Draw a bounding box around every artifact (stain precipitate or debris).
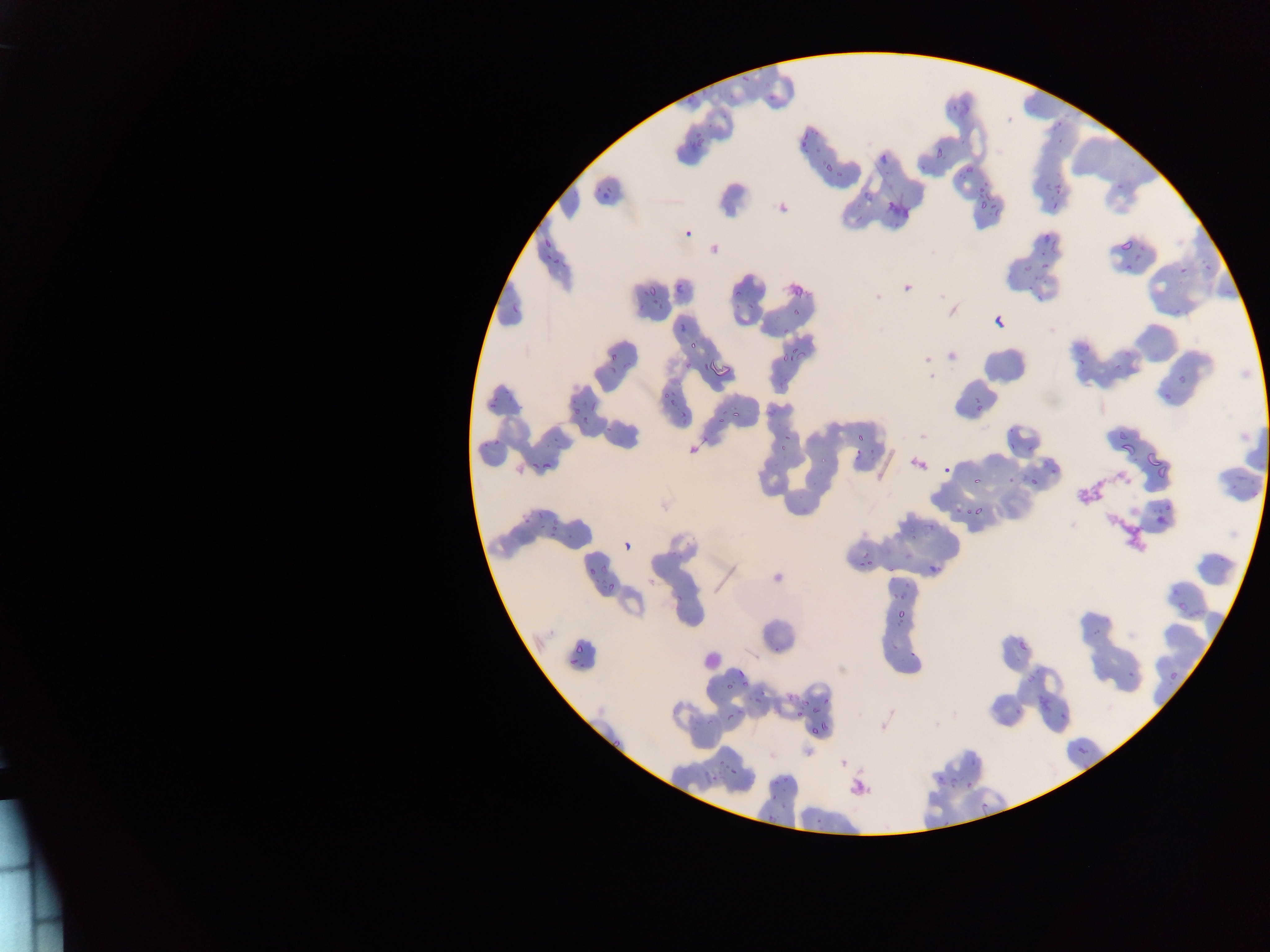

Approximate bounding boxes as (left, top, right, bottom) in pixels.
Artifacts (stain precipitate or debris): (884, 200, 908, 218), (783, 278, 806, 301), (1069, 474, 1108, 515), (1107, 510, 1150, 550), (846, 777, 868, 797).

Leukocyte locations: (700, 644, 726, 675). Malaria parasite locations: (740, 65, 756, 84), (686, 87, 704, 104), (770, 91, 777, 101), (727, 95, 737, 103), (946, 101, 960, 115), (704, 115, 719, 128), (1054, 116, 1063, 127), (686, 132, 709, 148), (794, 132, 811, 156), (1054, 135, 1062, 144), (932, 147, 944, 164), (876, 151, 890, 163), (823, 160, 838, 174), (962, 161, 983, 178), (918, 165, 927, 177), (1046, 174, 1064, 187), (596, 182, 611, 206), (976, 185, 995, 211), (861, 186, 876, 200), (1052, 202, 1060, 210), (683, 227, 694, 239), (1044, 231, 1051, 240), (1050, 235, 1061, 251), (1117, 235, 1135, 250), (544, 237, 553, 253), (543, 254, 551, 259), (551, 256, 561, 267), (1200, 259, 1211, 269), (1042, 260, 1054, 267), (1122, 264, 1132, 271), (1177, 265, 1187, 277), (675, 276, 687, 294), (639, 283, 656, 297), (1026, 283, 1034, 292), (729, 289, 741, 299), (1034, 293, 1042, 304), (651, 294, 667, 313), (744, 300, 759, 317), (511, 302, 516, 316), (1173, 302, 1183, 316), (789, 308, 803, 319), (994, 316, 1006, 329), (677, 319, 686, 331), (778, 344, 803, 369), (687, 345, 695, 351), (607, 347, 620, 360), (1075, 357, 1084, 367), (706, 360, 729, 380), (1112, 360, 1126, 372), (684, 362, 692, 370), (1175, 368, 1195, 383), (654, 379, 679, 403), (500, 391, 511, 397), (1162, 391, 1173, 400), (670, 396, 684, 414), (973, 396, 979, 404), (590, 399, 595, 410), (485, 400, 494, 409), (512, 404, 521, 411), (571, 407, 583, 415), (713, 408, 728, 430), (730, 408, 743, 422), (679, 411, 689, 423), (582, 413, 593, 424), (607, 423, 614, 431), (776, 431, 794, 454), (850, 431, 872, 455), (544, 432, 564, 445), (1007, 436, 1024, 450), (1118, 438, 1132, 453), (493, 439, 503, 444), (1028, 443, 1037, 452), (1145, 449, 1168, 468), (870, 450, 879, 462), (818, 453, 827, 463), (542, 460, 551, 467), (1152, 460, 1178, 482), (529, 461, 541, 469), (941, 464, 954, 475), (1049, 465, 1056, 474), (1029, 477, 1037, 487), (973, 481, 984, 488), (1159, 502, 1175, 514), (970, 504, 985, 518), (956, 505, 965, 513), (532, 510, 543, 522), (1153, 513, 1166, 526), (550, 514, 564, 533), (518, 518, 528, 526), (544, 524, 561, 540), (908, 527, 916, 539), (623, 541, 633, 551), (866, 556, 873, 566), (585, 558, 601, 575), (925, 560, 945, 579), (856, 561, 863, 570), (1171, 580, 1179, 593), (603, 583, 620, 593), (888, 587, 905, 601), (1177, 600, 1189, 613), (1189, 602, 1208, 620), (893, 604, 911, 623), (1014, 636, 1031, 657), (575, 638, 588, 657), (890, 641, 899, 650), (773, 645, 781, 655), (908, 648, 921, 658), (567, 660, 576, 667), (734, 668, 750, 686), (1126, 670, 1136, 678), (1169, 671, 1177, 683), (723, 682, 733, 695), (785, 689, 801, 703), (1034, 693, 1053, 713), (824, 695, 834, 702), (754, 696, 760, 706), (800, 696, 825, 718), (733, 702, 747, 715), (1013, 703, 1023, 716), (795, 713, 803, 724), (705, 715, 713, 725), (726, 715, 734, 722), (812, 717, 830, 737), (604, 737, 620, 750), (1075, 742, 1093, 762), (718, 757, 728, 766), (731, 764, 744, 775), (773, 774, 789, 786), (938, 774, 944, 785), (949, 775, 958, 785), (709, 776, 720, 784), (967, 778, 975, 788), (780, 799, 794, 810), (979, 801, 989, 812), (764, 809, 777, 828), (812, 813, 827, 821), (941, 821, 953, 827) | approximate (x, y) pixel centers of objects too small to bound: (1027, 267), (612, 370), (979, 407), (486, 445), (929, 528), (774, 797). Photographed through a microscope with a mobile-phone camera. Sample from Ghana. One field of view. Thin blood film. Image is 1270×952 pixels.